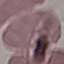 Result: negative for malaria parasites. Cell patch, automatically extracted from a larger field of view and resized to 64 × 64 pixels. Thin smear of blood. Giemsa stain. Acquired by smartphone through the microscope eyepiece.